Outline each Plasmodium ovale-infected red blood cell.
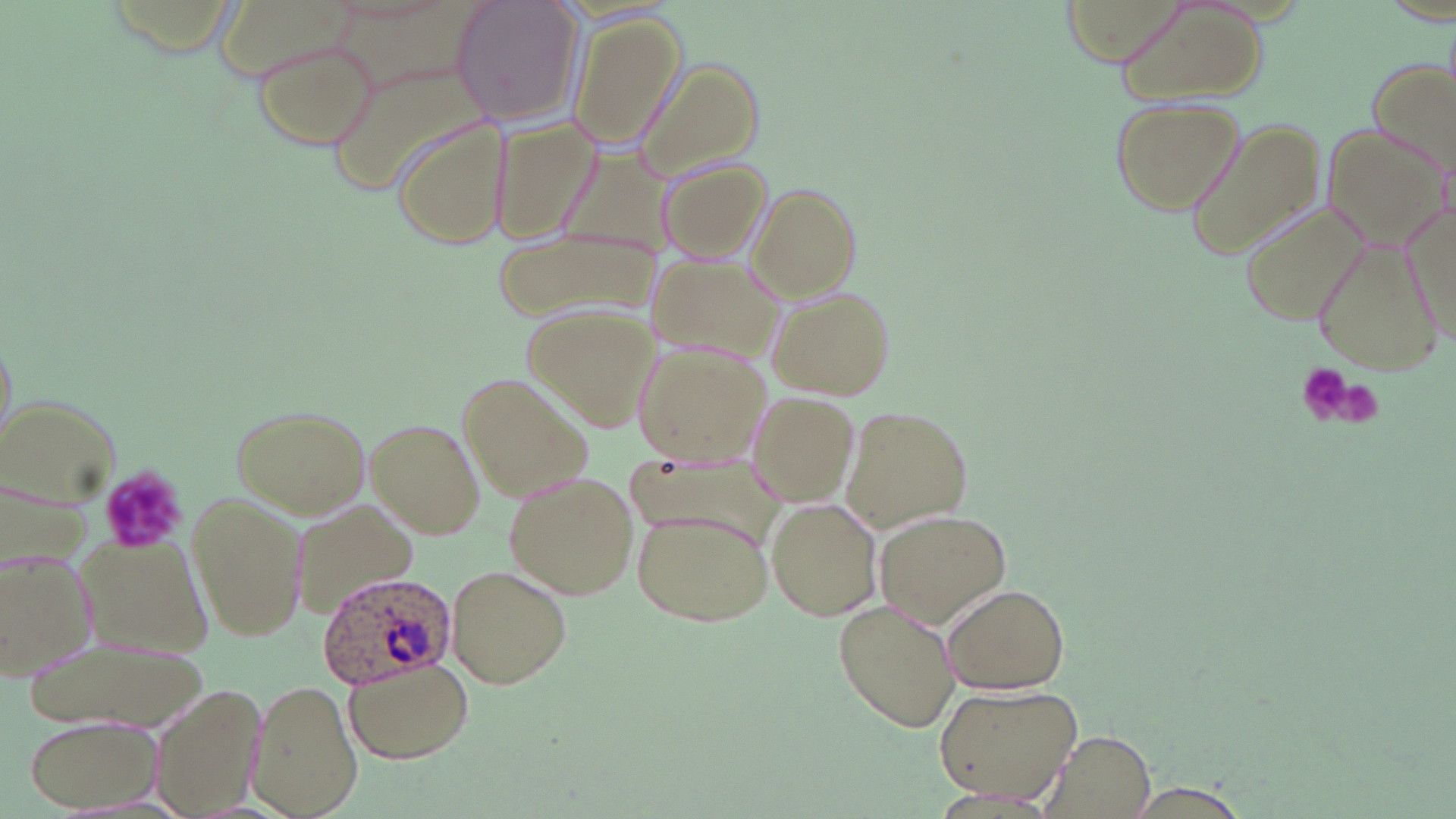
Approximate bounding boxes as named x1/y1/x2/y2 corners in pixels.
Plasmodium ovale-infected red blood cells: (x1=317, y1=571, x2=460, y2=690).

Summary:
  - Platelet locations: (x1=1294, y1=361, x2=1354, y2=422), (x1=1324, y1=377, x2=1387, y2=428), (x1=95, y1=467, x2=186, y2=555)
  - Uninfected red blood cell locations: (x1=450, y1=0, x2=581, y2=126), (x1=210, y1=2, x2=358, y2=84), (x1=332, y1=2, x2=503, y2=99), (x1=1117, y1=4, x2=1264, y2=105), (x1=565, y1=13, x2=685, y2=151), (x1=253, y1=39, x2=380, y2=151), (x1=1369, y1=54, x2=1455, y2=183), (x1=636, y1=58, x2=767, y2=185), (x1=330, y1=61, x2=496, y2=202), (x1=1109, y1=97, x2=1242, y2=214), (x1=392, y1=118, x2=511, y2=254), (x1=1182, y1=119, x2=1327, y2=267), (x1=491, y1=120, x2=605, y2=248), (x1=1322, y1=123, x2=1446, y2=250), (x1=552, y1=138, x2=689, y2=267), (x1=653, y1=153, x2=775, y2=266), (x1=745, y1=181, x2=864, y2=303), (x1=1238, y1=201, x2=1368, y2=329), (x1=490, y1=221, x2=656, y2=328), (x1=1312, y1=237, x2=1441, y2=374), (x1=642, y1=249, x2=787, y2=366), (x1=768, y1=285, x2=897, y2=401), (x1=527, y1=305, x2=657, y2=430), (x1=636, y1=339, x2=772, y2=464), (x1=459, y1=373, x2=594, y2=500), (x1=748, y1=392, x2=864, y2=508), (x1=1, y1=393, x2=124, y2=509), (x1=227, y1=402, x2=372, y2=519), (x1=840, y1=404, x2=972, y2=532), (x1=366, y1=416, x2=486, y2=539), (x1=622, y1=447, x2=786, y2=552), (x1=504, y1=471, x2=637, y2=602), (x1=188, y1=491, x2=306, y2=644), (x1=766, y1=499, x2=883, y2=622), (x1=296, y1=502, x2=418, y2=622), (x1=629, y1=507, x2=774, y2=629), (x1=873, y1=510, x2=1011, y2=627), (x1=73, y1=534, x2=214, y2=656), (x1=2, y1=548, x2=99, y2=680), (x1=445, y1=565, x2=573, y2=691), (x1=941, y1=582, x2=1072, y2=694), (x1=833, y1=599, x2=961, y2=733), (x1=30, y1=634, x2=208, y2=731), (x1=340, y1=655, x2=477, y2=764), (x1=147, y1=679, x2=264, y2=817), (x1=250, y1=680, x2=361, y2=819), (x1=934, y1=683, x2=1084, y2=807), (x1=23, y1=712, x2=162, y2=812), (x1=1039, y1=730, x2=1156, y2=819), (x1=1124, y1=782, x2=1251, y2=816)
  - Slide-level diagnosis: Plasmodium ovale
  - Modality: light microscopy
  - Field of view: single
  - Preparation: thin blood smear
  - Magnification: 1000x
  - Image size: 1456×819 pixels
  - Stain: May-Grünwald-Giemsa